State the blood parasite species.
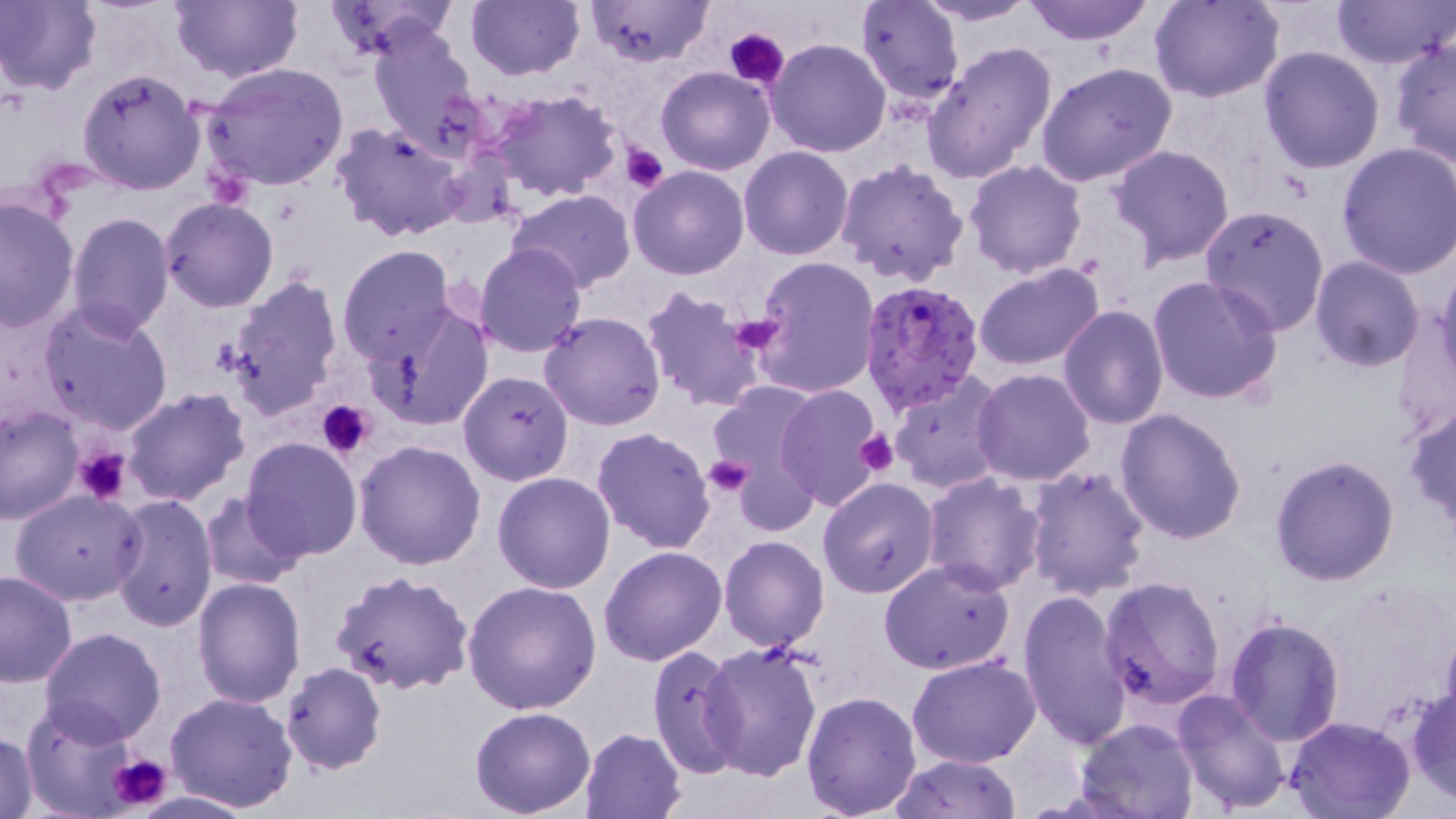

Plasmodium falciparum.

{
  "platelet_locations": "approximate bounding boxes as named x1/y1/x2/y2 corners in pixels: (x1=727, y1=28, x2=790, y2=88), (x1=620, y1=143, x2=670, y2=192), (x1=727, y1=310, x2=784, y2=356), (x1=317, y1=399, x2=376, y2=459), (x1=856, y1=430, x2=901, y2=477), (x1=75, y1=445, x2=133, y2=505), (x1=702, y1=455, x2=753, y2=496), (x1=107, y1=751, x2=173, y2=815)",
  "preparation": "thin blood film",
  "plasmodium_falciparum_infected_red_blood_cell_locations": "approximate bounding boxes as named x1/y1/x2/y2 corners in pixels: (x1=858, y1=278, x2=985, y2=415)",
  "modality": "optical microscopy",
  "uninfected_red_blood_cell_locations": "approximate bounding boxes as named x1/y1/x2/y2 corners in pixels: (x1=0, y1=0, x2=101, y2=96), (x1=322, y1=0, x2=460, y2=60), (x1=464, y1=0, x2=583, y2=81), (x1=858, y1=0, x2=964, y2=104), (x1=912, y1=0, x2=1042, y2=26), (x1=1022, y1=0, x2=1155, y2=45), (x1=1151, y1=0, x2=1283, y2=103), (x1=1331, y1=0, x2=1452, y2=71), (x1=169, y1=1, x2=304, y2=84), (x1=585, y1=1, x2=713, y2=68), (x1=368, y1=24, x2=483, y2=153), (x1=768, y1=37, x2=891, y2=156), (x1=1389, y1=38, x2=1455, y2=170), (x1=921, y1=40, x2=1059, y2=183), (x1=1259, y1=45, x2=1386, y2=173), (x1=201, y1=61, x2=350, y2=192), (x1=1036, y1=61, x2=1178, y2=188), (x1=76, y1=67, x2=205, y2=194), (x1=656, y1=67, x2=775, y2=176), (x1=490, y1=91, x2=623, y2=202), (x1=331, y1=120, x2=467, y2=243), (x1=1337, y1=142, x2=1456, y2=278), (x1=1108, y1=143, x2=1236, y2=266), (x1=739, y1=147, x2=853, y2=260), (x1=835, y1=157, x2=970, y2=287), (x1=964, y1=159, x2=1088, y2=278), (x1=627, y1=165, x2=748, y2=280), (x1=508, y1=188, x2=637, y2=293), (x1=0, y1=196, x2=79, y2=333), (x1=160, y1=198, x2=279, y2=313), (x1=1199, y1=205, x2=1329, y2=336), (x1=67, y1=211, x2=174, y2=335), (x1=474, y1=242, x2=589, y2=357), (x1=337, y1=246, x2=457, y2=365), (x1=750, y1=255, x2=880, y2=399), (x1=1309, y1=256, x2=1427, y2=372), (x1=1436, y1=261, x2=1456, y2=387), (x1=974, y1=263, x2=1105, y2=372), (x1=225, y1=273, x2=343, y2=417), (x1=1148, y1=275, x2=1282, y2=406), (x1=641, y1=285, x2=766, y2=412), (x1=35, y1=299, x2=174, y2=434), (x1=366, y1=303, x2=494, y2=432), (x1=1059, y1=303, x2=1170, y2=428), (x1=539, y1=311, x2=666, y2=431), (x1=972, y1=368, x2=1096, y2=485), (x1=458, y1=371, x2=574, y2=486), (x1=890, y1=373, x2=1007, y2=495), (x1=708, y1=379, x2=825, y2=516), (x1=775, y1=383, x2=887, y2=511), (x1=121, y1=387, x2=252, y2=507), (x1=0, y1=405, x2=84, y2=524), (x1=1403, y1=405, x2=1456, y2=531), (x1=1115, y1=408, x2=1248, y2=543), (x1=590, y1=426, x2=717, y2=553), (x1=240, y1=435, x2=363, y2=561), (x1=355, y1=438, x2=487, y2=571), (x1=1268, y1=455, x2=1399, y2=586), (x1=1022, y1=465, x2=1151, y2=604), (x1=493, y1=472, x2=616, y2=592), (x1=922, y1=472, x2=1049, y2=595), (x1=818, y1=478, x2=940, y2=599), (x1=11, y1=489, x2=145, y2=606), (x1=109, y1=492, x2=217, y2=633), (x1=197, y1=493, x2=303, y2=591), (x1=718, y1=536, x2=830, y2=654), (x1=599, y1=545, x2=727, y2=665), (x1=878, y1=560, x2=1017, y2=676), (x1=0, y1=570, x2=78, y2=688), (x1=329, y1=570, x2=475, y2=697), (x1=1098, y1=575, x2=1227, y2=708), (x1=192, y1=576, x2=306, y2=706), (x1=462, y1=581, x2=604, y2=715), (x1=1018, y1=590, x2=1132, y2=748), (x1=1224, y1=615, x2=1345, y2=745), (x1=38, y1=627, x2=167, y2=746), (x1=696, y1=640, x2=823, y2=782), (x1=648, y1=644, x2=745, y2=779), (x1=906, y1=656, x2=1041, y2=768), (x1=280, y1=662, x2=386, y2=774), (x1=1408, y1=684, x2=1456, y2=802), (x1=801, y1=689, x2=923, y2=817), (x1=1171, y1=689, x2=1291, y2=814), (x1=165, y1=691, x2=298, y2=812), (x1=22, y1=702, x2=145, y2=815), (x1=469, y1=706, x2=597, y2=818), (x1=1284, y1=715, x2=1417, y2=819), (x1=1074, y1=717, x2=1199, y2=819), (x1=579, y1=727, x2=687, y2=817), (x1=1, y1=731, x2=40, y2=817), (x1=889, y1=753, x2=1023, y2=818)",
  "field_of_view": "single",
  "stain": "May-Grünwald-Giemsa",
  "magnification": "1000x",
  "image_size": "1456×819 pixels"
}